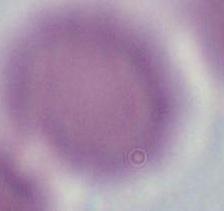 Photomicrograph. Captured at 1000x magnification. An erythrocyte is seen.